Identify the blood parasite species.
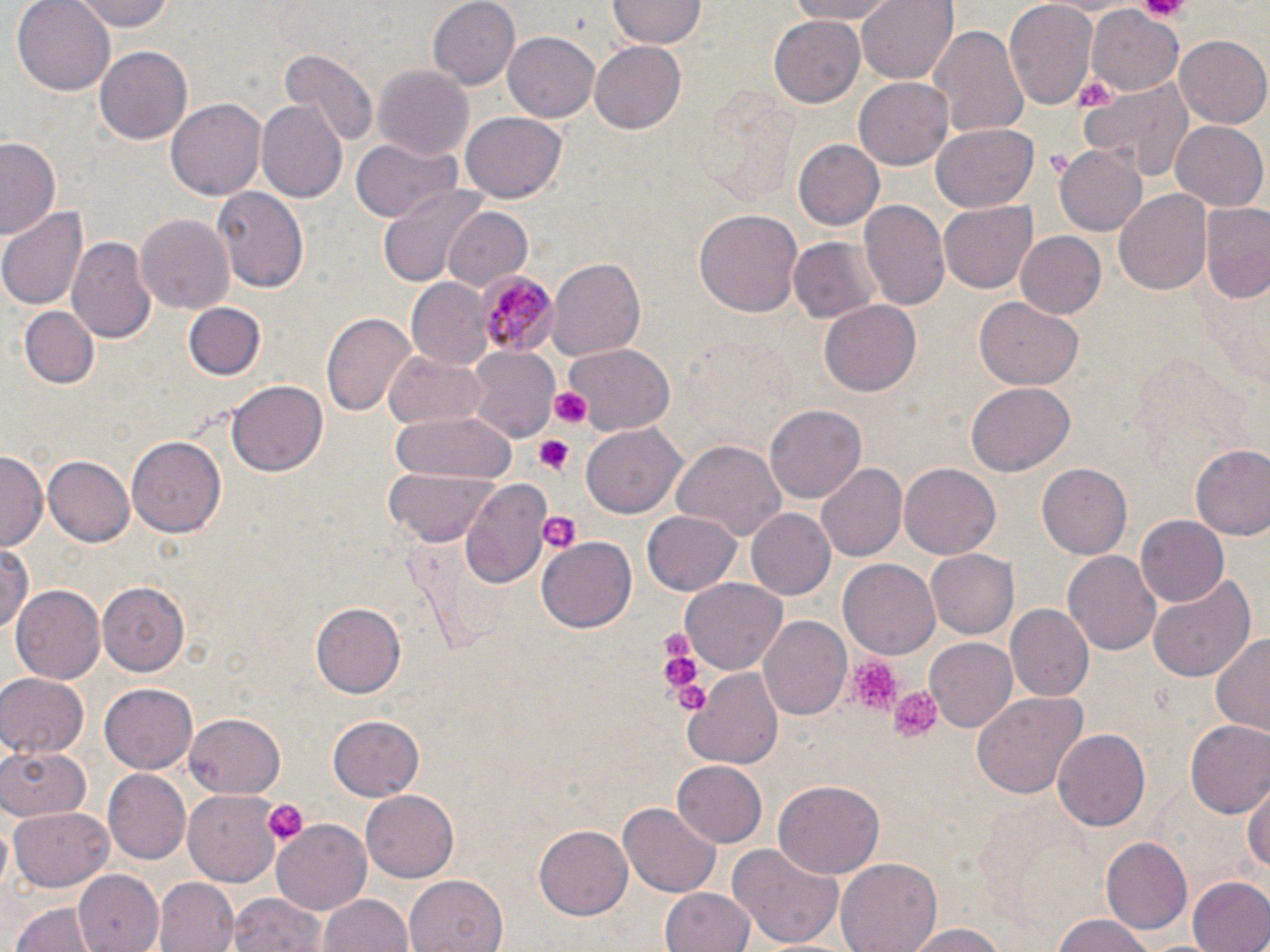

Plasmodium malariae.

Approximate bounding boxes as (x1,y1)-(x2,y2) corner pairs in pixels. Platelet locations: (1139,0)-(1190,20), (548,387)-(592,429), (532,434)-(576,473), (539,510)-(581,555), (657,632)-(702,693), (848,657)-(903,716), (664,666)-(712,718), (887,684)-(945,743), (263,799)-(308,846). Plasmodium malariae-infected red blood cell locations: (475,269)-(555,358). Uninfected red blood cell locations: (10,0)-(117,93), (71,0)-(173,31), (427,0)-(521,90), (610,0)-(706,46), (780,0)-(899,24), (858,0)-(958,83), (1006,0)-(1099,111), (1087,5)-(1185,93), (769,11)-(865,105), (929,23)-(1028,138), (503,32)-(598,123), (1174,35)-(1269,126), (590,40)-(685,134), (94,45)-(195,145), (279,50)-(377,150), (373,66)-(471,159), (1081,76)-(1194,181), (855,78)-(956,168), (166,98)-(265,201), (259,100)-(348,203), (461,112)-(565,203), (1170,121)-(1268,210), (930,124)-(1039,213), (1,135)-(62,240), (354,138)-(460,224), (793,139)-(884,230), (1055,141)-(1149,235), (212,186)-(309,294), (376,187)-(489,290), (1115,188)-(1212,295), (860,200)-(949,314), (939,201)-(1036,294), (1199,202)-(1270,302), (1,205)-(87,310), (440,206)-(535,290), (693,208)-(802,318), (138,213)-(234,317), (1014,230)-(1107,318), (67,236)-(154,341), (788,236)-(880,323), (546,258)-(646,362), (405,278)-(499,370), (974,299)-(1084,390), (820,300)-(922,398), (186,303)-(264,380), (18,306)-(99,389), (320,310)-(418,416), (562,343)-(676,434), (468,347)-(560,443), (383,352)-(486,429), (228,377)-(327,474), (966,381)-(1075,474), (766,404)-(866,505), (390,410)-(514,488), (581,424)-(684,518), (129,435)-(225,538), (673,439)-(787,539), (1190,443)-(1270,540), (0,453)-(44,549), (43,455)-(135,546), (816,462)-(908,562), (899,462)-(1001,558), (1038,464)-(1132,559), (383,467)-(498,544), (459,478)-(553,591), (642,509)-(740,594), (745,509)-(836,600), (1136,516)-(1228,608), (538,538)-(636,630), (0,542)-(35,633), (1063,549)-(1161,655), (927,550)-(1019,638), (840,558)-(943,659), (1148,574)-(1254,685), (682,578)-(786,674), (97,580)-(191,674), (11,585)-(103,685), (310,603)-(404,697), (1008,603)-(1091,698), (759,615)-(851,720), (1210,632)-(1270,738), (925,639)-(1018,731), (684,667)-(782,768), (0,672)-(89,757), (100,681)-(199,770), (968,690)-(1085,800), (184,713)-(286,799), (327,715)-(425,800), (1185,721)-(1270,820), (1053,730)-(1152,829), (0,745)-(92,822), (672,761)-(767,847), (104,771)-(190,865), (775,779)-(884,878), (1247,779)-(1270,879), (184,789)-(282,882), (359,789)-(461,883), (621,802)-(719,897), (8,806)-(116,891), (273,820)-(373,915), (533,826)-(630,920), (1101,837)-(1192,934), (729,841)-(844,949), (836,859)-(943,952), (75,870)-(163,952), (404,875)-(507,952), (1187,877)-(1270,952), (153,878)-(238,952), (660,887)-(758,952), (230,892)-(326,952), (319,893)-(412,952), (11,900)-(98,952), (1048,916)-(1161,952), (902,922)-(1014,952). Thin blood film. Image is 1270×952 pixels. Optical microscopy. May-Grünwald-Giemsa-stained preparation. One field of a larger specimen. 1000x magnification.